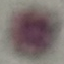
Summary:
  - Malaria status: uninfected
  - Stain: Giemsa
  - Image type: automatically extracted cell patch, resized to 64 × 64 pixels
  - Preparation: thin smear
  - Capture: smartphone camera at the microscope eyepiece